Comment on the background quality.
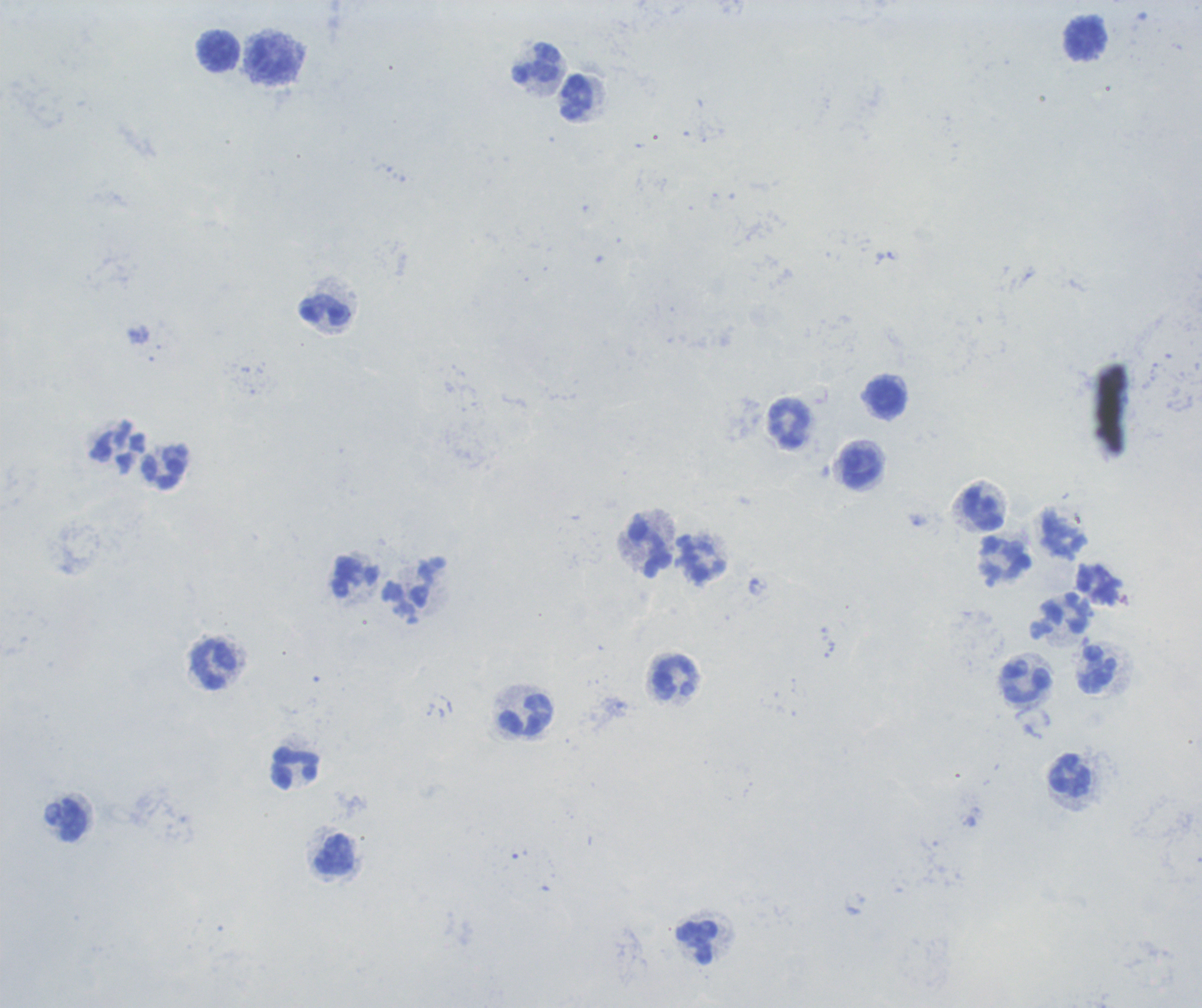
Unsatisfactory.

Approximate centers as (x, y) in pixels.
Summary:
  - Leukocyte locations: (1086, 40), (220, 53), (274, 60), (538, 65), (577, 98), (326, 312), (888, 397), (790, 425), (862, 469), (165, 470), (983, 509), (651, 548), (1004, 562), (1062, 616), (214, 665), (1097, 670), (675, 678), (1025, 683), (526, 716), (296, 769), (1070, 776), (72, 820), (335, 854), (697, 943)
  - Field of view: single
  - Result: no Plasmodium parasites seen
  - Magnification: 100x
  - Stain: Romanowsky
  - Preparation: thick blood smear
  - Context: previously used in an actual diagnosis
  - Image size: 1202×1008 pixels